Name the cell type shown.
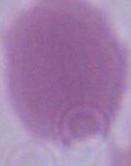
An erythrocyte.

Summary:
  - Magnification: 1000x
  - Modality: micrograph